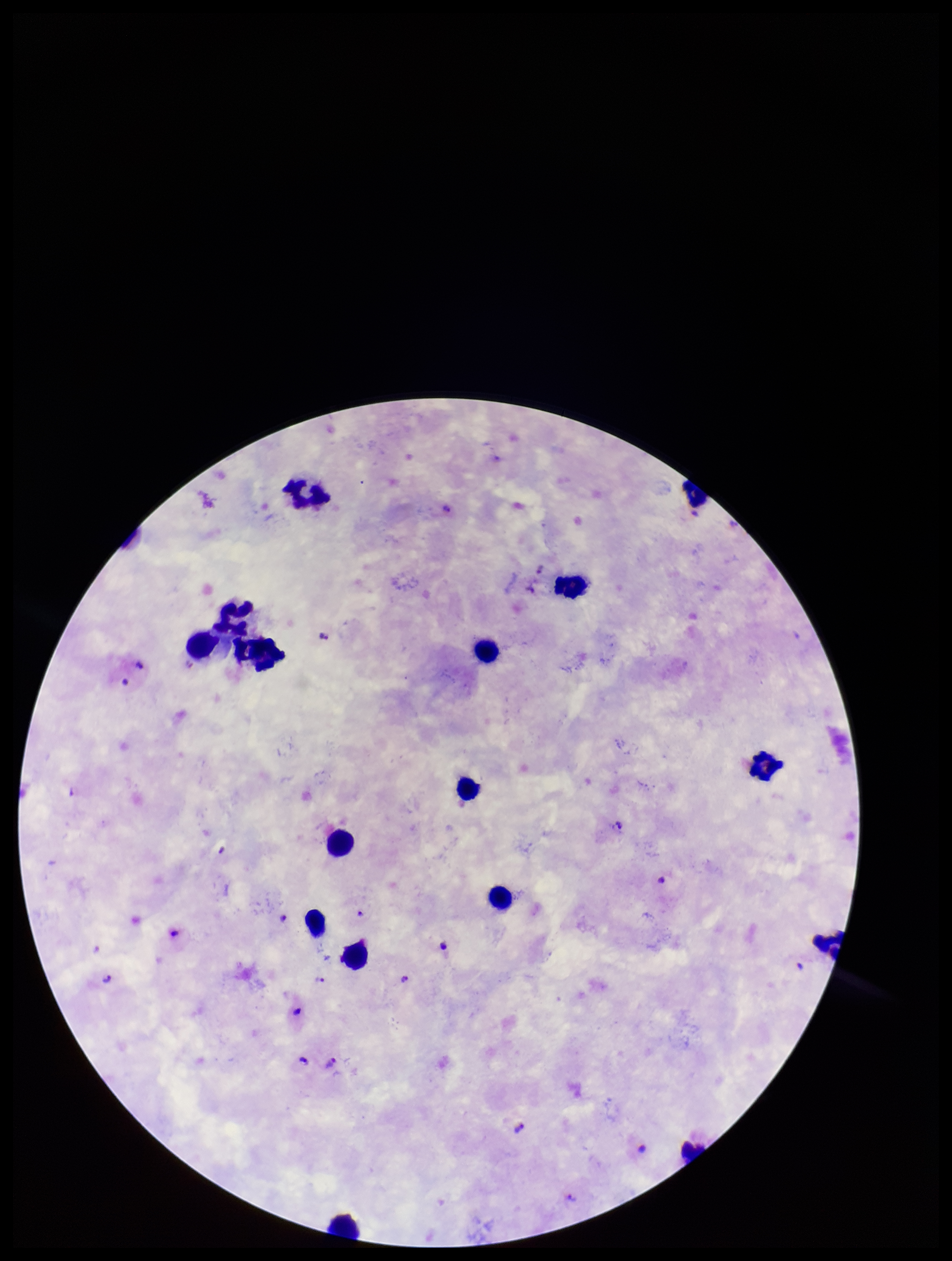

Summary:
  - Field of view: one from this slide
  - Capture: smartphone photograph through the microscope eyepiece
  - Plasmodium parasites: seen
  - Preparation: thick
  - Stain: Giemsa
  - Parasite count: 12
  - Leukocyte count: 16
  - Image size: 952×1261 pixels
  - Species reported for this patient: Plasmodium falciparum
  - Patient malaria status: positive